Comment on the morphology of the red blood cells.
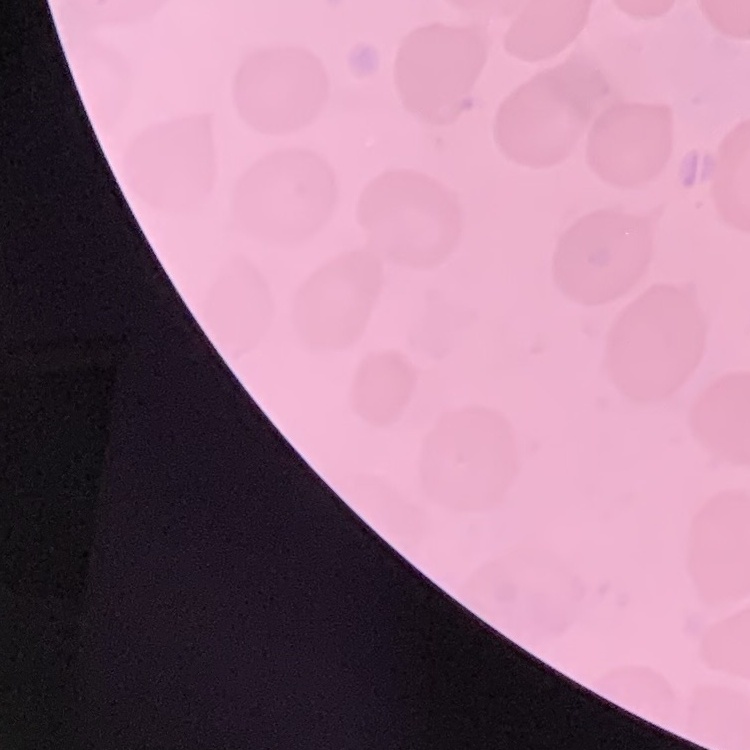

They show no rouleaux formation.

Stained with either Field's or Giemsa. Thin peripheral smear. Square crop of a larger photomicrograph.